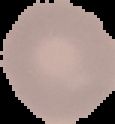

Summary:
  - Preparation: thin blood smear
  - Image size: 115×124 pixels
  - Image type: segmented cell region with the area outside set to black
  - Result: no Plasmodium parasites seen